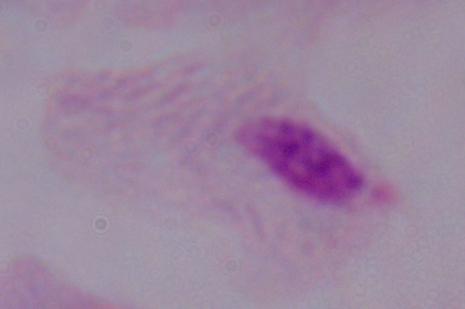
Photomicrograph. A trichomonad is seen. Captured at 1000x magnification.